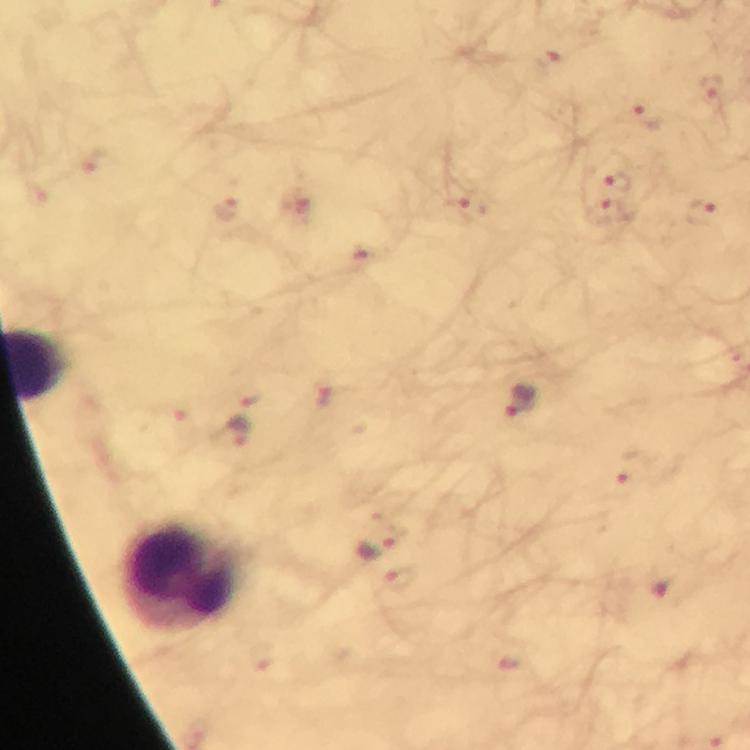

Approximate object centers, in pixels from the top-left corner.
Summary:
  - Malaria parasite locations: (x=546, y=61), (x=712, y=89), (x=643, y=117), (x=620, y=181), (x=298, y=205), (x=464, y=210), (x=228, y=212), (x=608, y=212), (x=701, y=212), (x=361, y=259), (x=249, y=395), (x=326, y=400), (x=521, y=404), (x=236, y=432), (x=633, y=473), (x=376, y=547), (x=402, y=579)
  - Leukocyte locations: (x=182, y=575)
  - Magnification: 100x
  - Immersion oil: applied
  - Capture: smartphone camera through the microscope
  - Cropped from: a single field of view
  - Preparation: thick blood film
  - Stain: Giemsa
  - Context: from a malaria diagnostic workup
  - Image size: 750×750 pixels